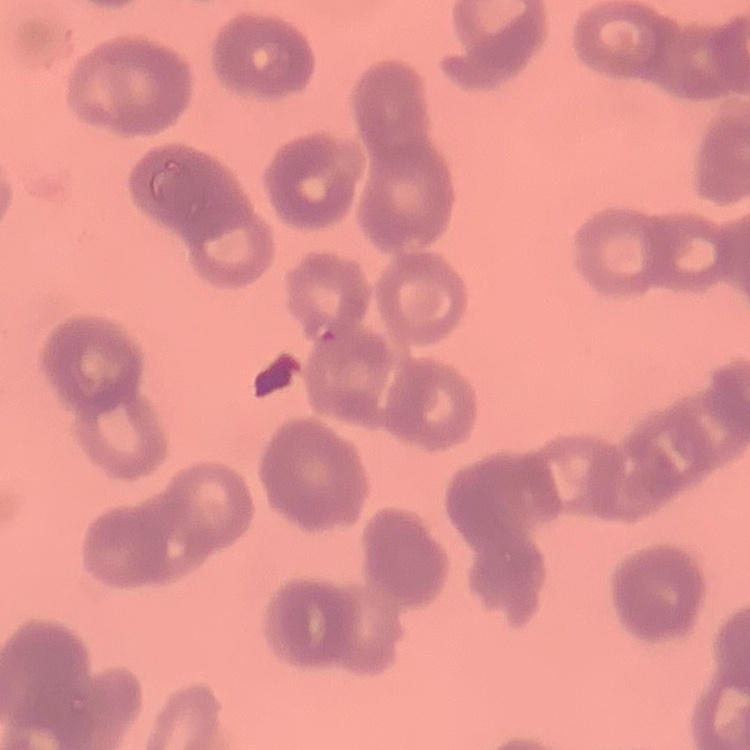

erythrocyte_morphology: rouleaux formation
image_type: square crop of a larger photomicrograph
preparation: thin peripheral smear
stain: Field's or Giemsa